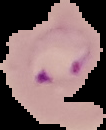

Image is 106×130 pixels. From a thin blood smear. Result: Plasmodium parasites identified. The area outside the segmented cell region is set to black.